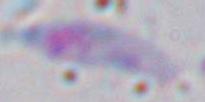
{
  "modality": "micrograph",
  "identification": "Toxoplasma gondii",
  "magnification": "1000x"
}